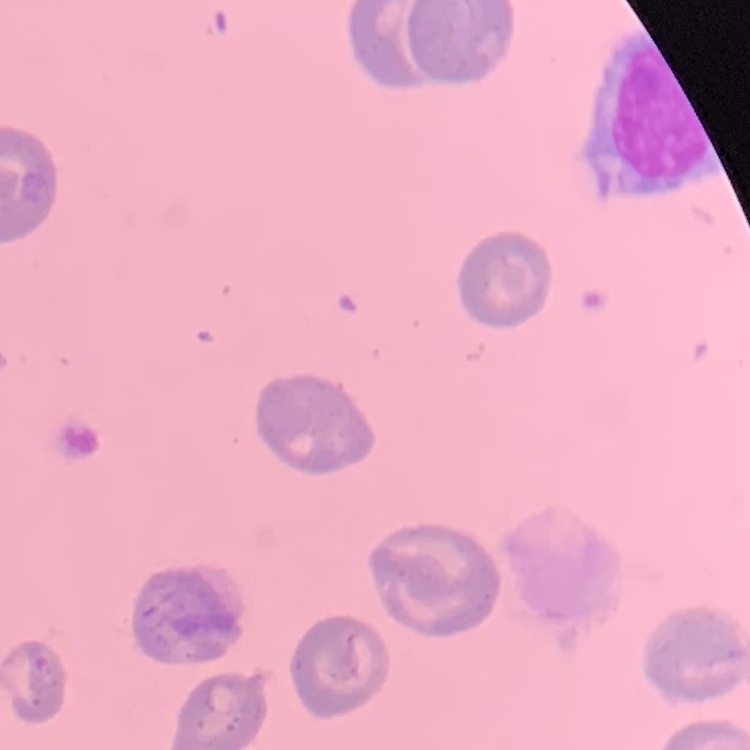

{
  "red_blood_cell_morphology": "no rouleaux formation",
  "stain": "Field's or Giemsa",
  "image_type": "one tile cut from a larger photomicrograph",
  "preparation": "thin peripheral smear"
}